Give the preparation type.
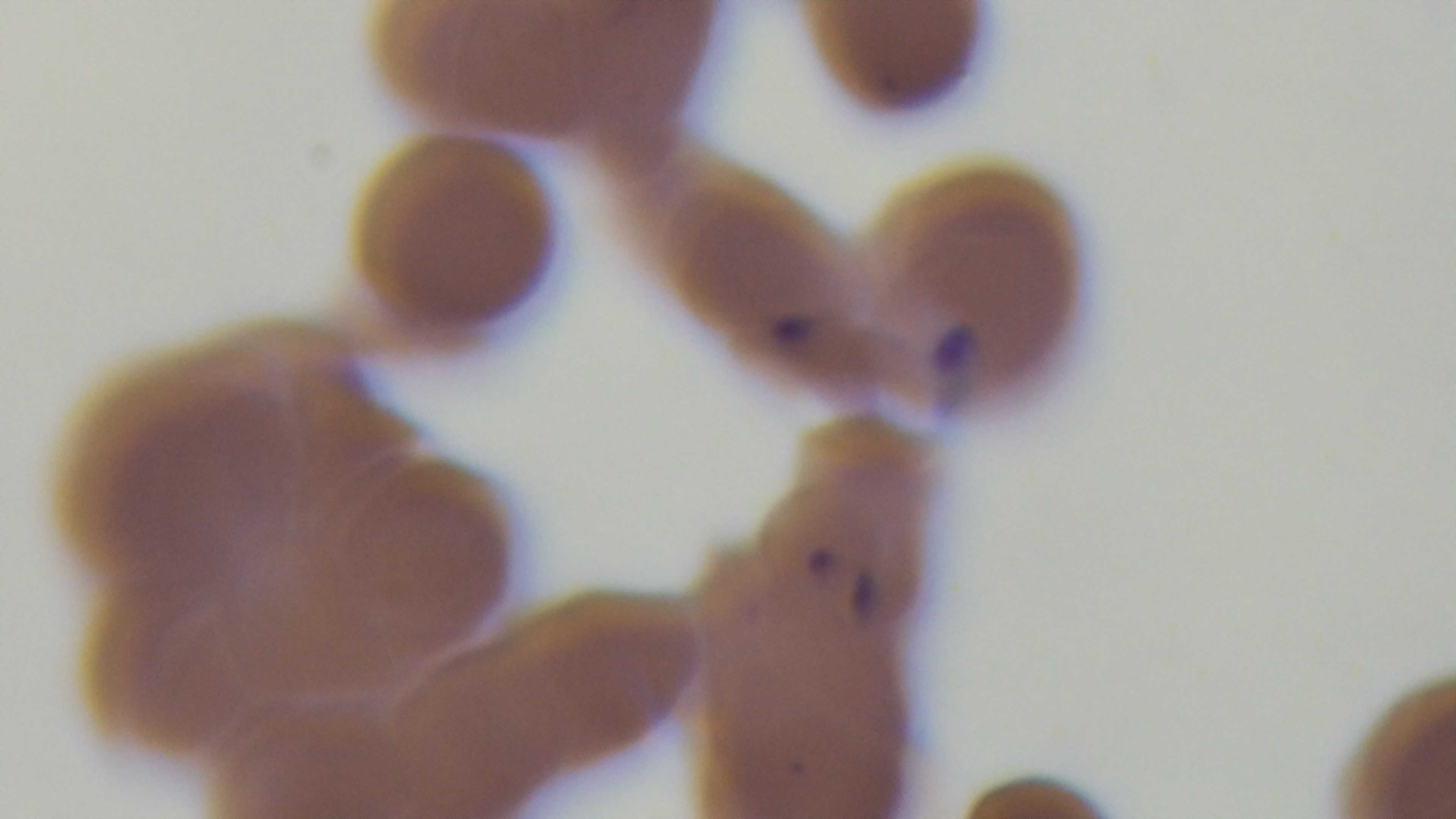
A thin smear.

Malaria status: infected. Single field of view. Giemsa stain. Oil-immersion objective, 100x. Light microscopy. Captured with a mounted 4K digital camera.